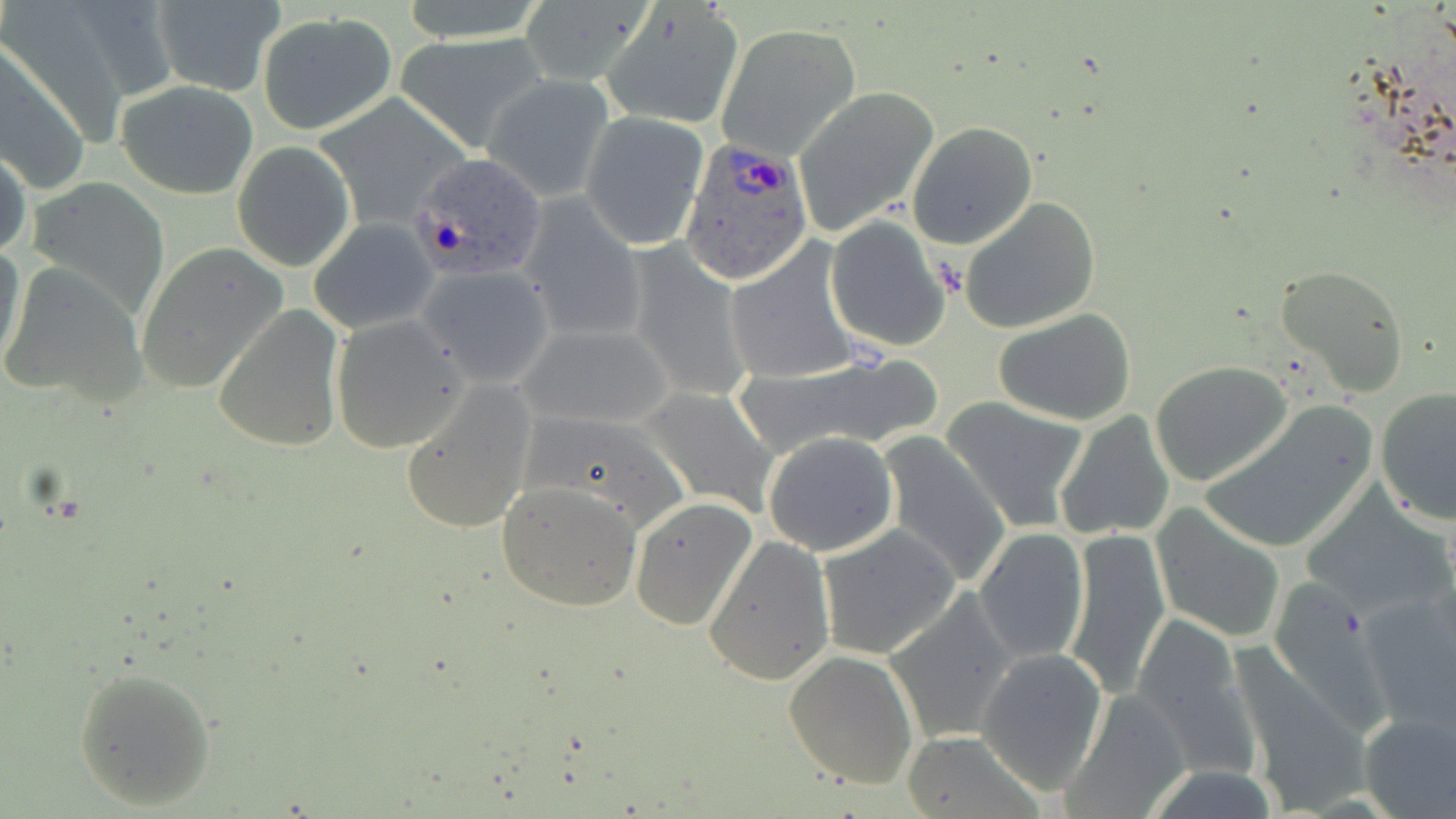

Summary:
  - Coordinate format: approximate bounding boxes as [x1, y1, x2, y2] in pixels
  - Plasmodium ovale-infected red blood cell locations: [676, 134, 815, 286], [405, 151, 549, 284]
  - Uninfected red blood cell locations: [519, 0, 652, 87], [151, 1, 285, 95], [603, 5, 746, 130], [256, 12, 398, 135], [715, 25, 859, 162], [397, 34, 553, 151], [0, 44, 89, 195], [484, 75, 616, 201], [117, 79, 258, 199], [792, 87, 939, 237], [314, 94, 470, 229], [580, 111, 710, 249], [906, 122, 1036, 249], [232, 142, 355, 271], [0, 146, 31, 261], [27, 177, 170, 313], [518, 195, 646, 344], [958, 196, 1102, 335], [825, 216, 953, 352], [309, 220, 439, 336], [0, 237, 27, 377], [724, 241, 862, 385], [624, 242, 752, 404], [136, 243, 289, 394], [0, 262, 148, 409], [417, 264, 557, 388], [1275, 264, 1411, 397], [213, 306, 344, 454], [993, 307, 1138, 426], [331, 316, 468, 453], [515, 322, 678, 430], [736, 351, 946, 459], [1151, 360, 1294, 486], [399, 380, 540, 536], [638, 385, 779, 522], [1375, 385, 1456, 526], [943, 397, 1092, 533], [1202, 404, 1379, 553], [522, 408, 691, 532], [1053, 409, 1178, 541], [762, 431, 900, 557], [877, 434, 1012, 587], [497, 481, 643, 611], [629, 496, 757, 632], [1301, 500, 1451, 622], [1150, 503, 1285, 643], [817, 522, 962, 659], [975, 528, 1089, 664], [1063, 528, 1170, 698], [703, 533, 836, 686], [1354, 586, 1456, 728], [885, 590, 1020, 742], [1125, 615, 1258, 773], [976, 648, 1110, 793], [783, 651, 918, 790], [73, 667, 215, 809], [1057, 690, 1191, 819], [1357, 709, 1455, 818], [900, 730, 1042, 819], [1137, 765, 1284, 819]
  - Slide-level diagnosis: Plasmodium ovale
  - Field of view: one of a larger specimen
  - Stain: May-Grünwald-Giemsa
  - Preparation: thin blood smear
  - Image size: 1456×819 pixels
  - Modality: light microscopy
  - Magnification: 1000x